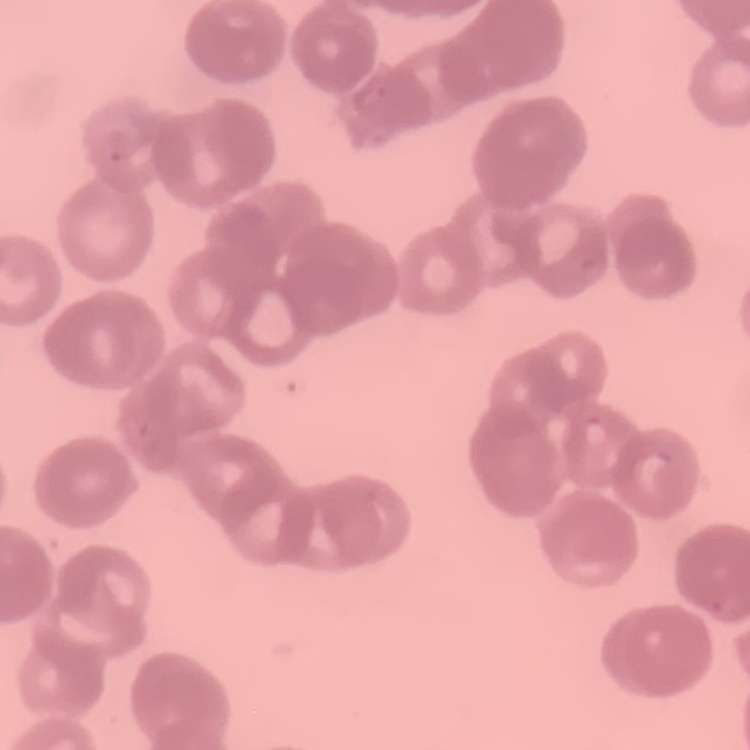

Summary:
  - Erythrocyte morphology: rouleaux formation
  - Image type: one tile cut from a larger photomicrograph
  - Stain: Field's or Giemsa
  - Preparation: thin peripheral smear